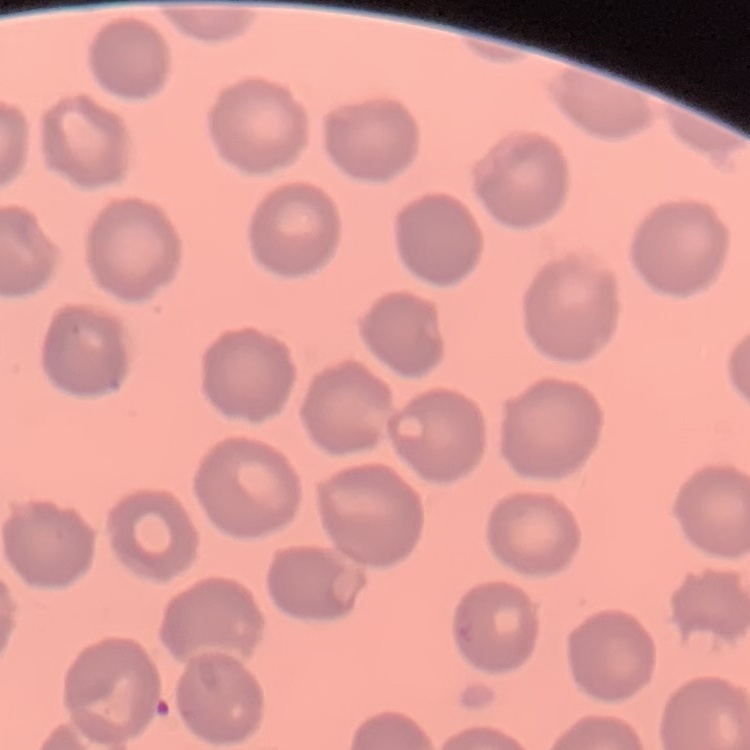
The erythrocytes show no rouleaux formation. One tile cut from a larger photomicrograph. Thin blood film. Stained with either Field's or Giemsa.